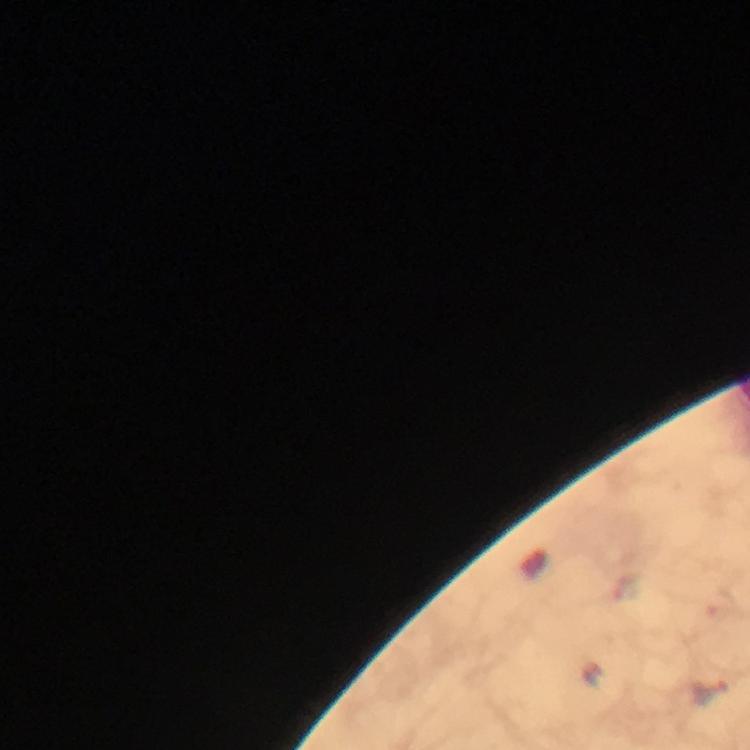
cropped from = one field of view
magnification = 100x
stain = Giemsa
preparation = thick smear
malaria parasite locations = approximate object centers, in pixels from the top-left corner: (x=591, y=673), (x=710, y=691)
capture = smartphone mounted on the microscope
image size = 750×750 pixels
immersion oil = applied
context = from a diagnostic examination for malaria